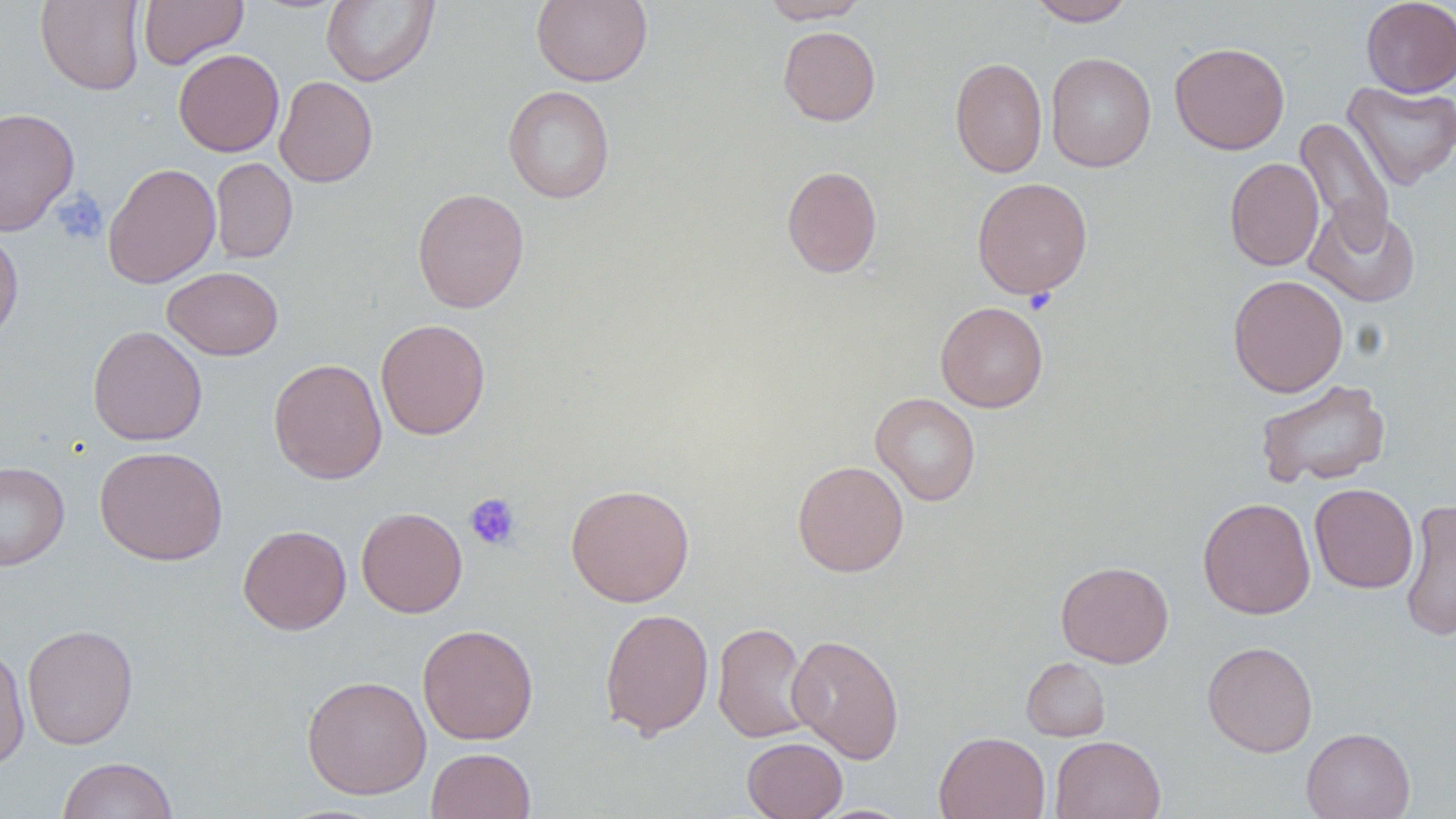

slide-level diagnosis = negative for blood parasites
field of view = single
platelet locations = approximate bounding boxes as (x1,y1)-(x2,y2) corner pairs in pixels: (53,189)-(108,246), (463,492)-(522,551)
modality = optical microscopy
preparation = thin blood film
magnification = 1000x
stain = May-Grünwald-Giemsa
uninfected red blood cell locations = approximate bounding boxes as (x1,y1)-(x2,y2) corner pairs in pixels: (139,0)-(249,69), (320,0)-(439,87), (531,0)-(653,87), (761,0)-(871,23), (1026,0)-(1136,25), (1360,0)-(1456,98), (36,1)-(145,95), (778,25)-(881,126), (1169,42)-(1290,154), (173,49)-(285,157), (1045,52)-(1156,171), (950,57)-(1048,178), (275,76)-(378,188), (1342,81)-(1456,190), (503,85)-(615,204), (0,107)-(79,235), (1294,116)-(1396,251), (211,157)-(297,263), (1224,157)-(1324,271), (102,163)-(221,288), (782,165)-(883,278), (971,177)-(1093,299), (412,187)-(529,313), (1305,202)-(1421,307), (0,227)-(23,345), (163,266)-(284,360), (1227,274)-(1349,397), (936,301)-(1048,412), (375,318)-(490,440), (87,325)-(207,446), (268,358)-(387,484), (1255,378)-(1391,488), (871,393)-(980,506), (95,445)-(228,565), (792,460)-(909,577), (0,461)-(69,570), (565,483)-(695,607), (1310,483)-(1419,593), (1197,496)-(1316,619), (1400,499)-(1456,643), (356,507)-(467,618), (238,525)-(351,635), (1056,561)-(1173,668), (600,607)-(715,740), (713,622)-(814,743), (22,624)-(138,749), (417,624)-(539,744), (786,634)-(905,764), (1202,641)-(1318,757), (0,644)-(31,771), (1022,657)-(1111,741), (302,675)-(431,799), (1301,727)-(1415,819), (934,731)-(1050,819), (1050,735)-(1165,819), (742,736)-(848,819), (426,747)-(535,819), (58,756)-(178,818)
image size = 1456×819 pixels